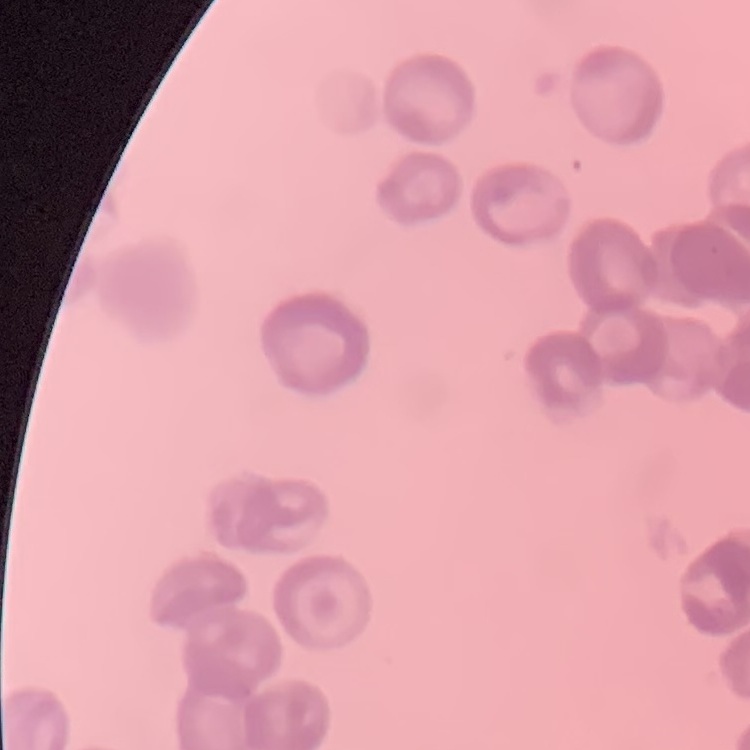

The erythrocytes show rouleaux formation. Field's or Giemsa stain. Thin blood smear. Square crop of a larger photomicrograph.